Name the cell type shown.
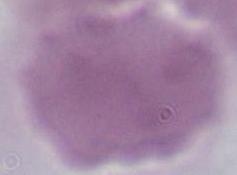

This is an erythrocyte.

Captured at 1000x magnification. Micrograph.